Assess this cell for malaria.
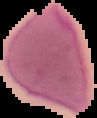

Uninfected.

Summary:
  - Image type: segmented cell region with the area outside set to black
  - Preparation: thin blood smear
  - Image size: 97×118 pixels